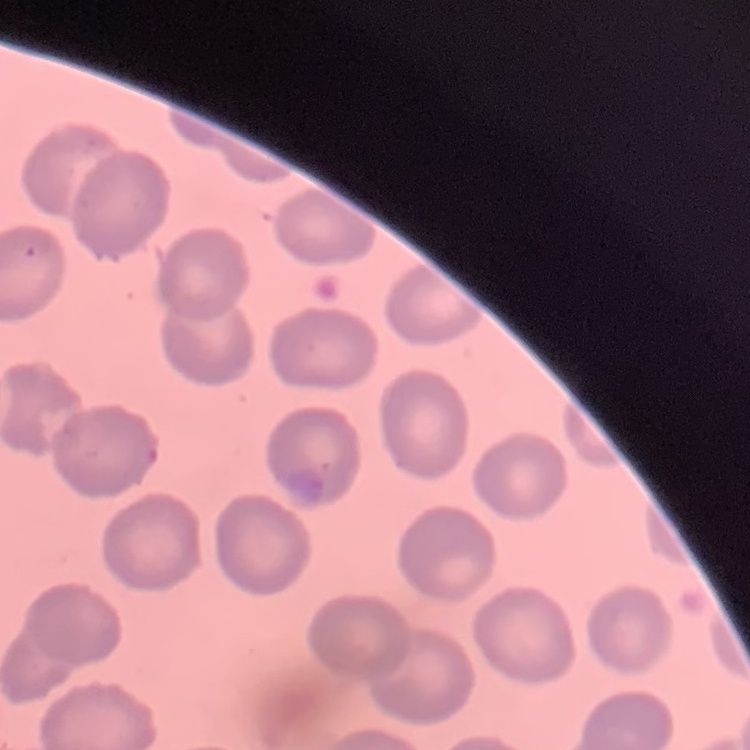
The red blood cells exhibit no rouleaux formation. One tile cut from a larger photomicrograph. Stained with either Field's or Giemsa. Thin blood smear.